Give the position of every Plasmodium parasite visible.
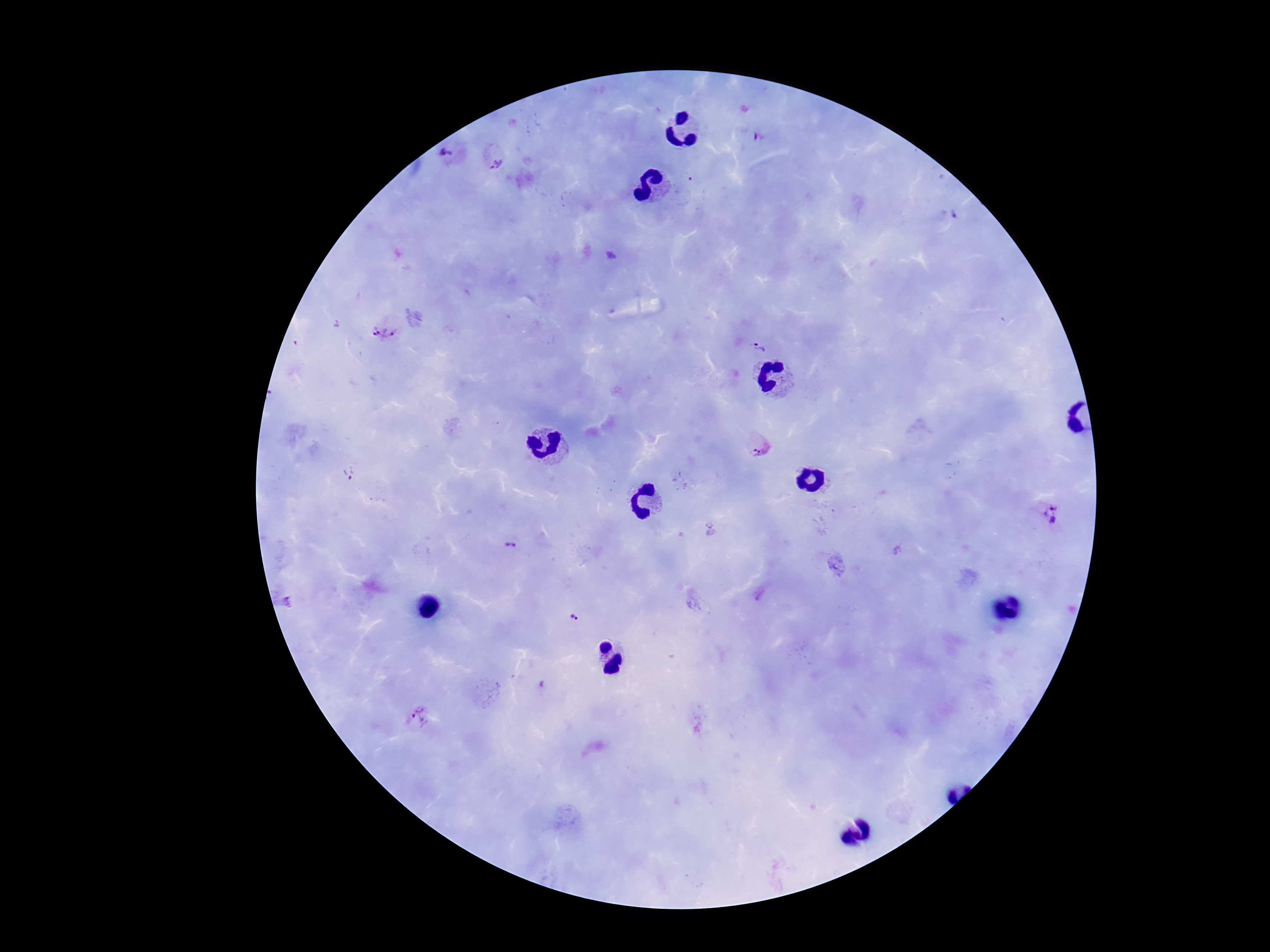
Approximate centers as (x, y) in pixels.
Plasmodium parasites: (452, 156), (496, 159), (386, 328), (759, 348), (760, 445), (351, 474), (1052, 516), (509, 546), (287, 602), (573, 618), (421, 716).

Summary:
  - Stain: Giemsa
  - Field of view: one from this slide
  - Image size: 1270×952 pixels
  - Preparation: thick peripheral-blood smear
  - Magnification: 100x
  - Capture: smartphone camera through the microscope eyepiece
  - Patient malaria status: infected